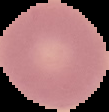

Summary:
  - Preparation: thin blood film
  - Image size: 109×112 pixels
  - Malaria status: uninfected
  - Image type: segmented cell region with the area outside set to black